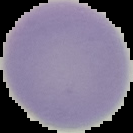

image_size: 133×133 pixels
malaria_status: uninfected
image_type: cell region segmented out of the field of view; surrounding area masked to black
preparation: thin blood film